Assess this cell for malaria.
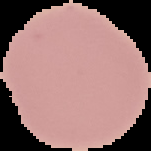

It is uninfected.

Summary:
  - Image size: 151×151 pixels
  - Preparation: thin blood film
  - Image type: segmented cell region with the area outside set to black